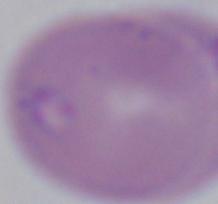
Summary:
  - Magnification: 1000x
  - Identification: Babesia
  - Modality: micrograph